Classify this cell by malaria status.
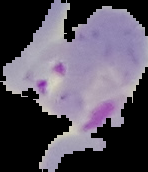

It is parasitized.

Summary:
  - Image type: segmented cell region on a black background
  - Preparation: thin blood film
  - Image size: 148×172 pixels